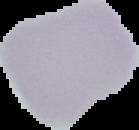

Summary:
  - Malaria status: uninfected
  - Image type: segmented cell region on a black background
  - Image size: 139×130 pixels
  - Preparation: thin blood smear